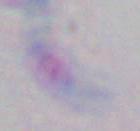
magnification = 1000x
identification = Toxoplasma gondii
modality = photomicrograph